Identify the parasite.
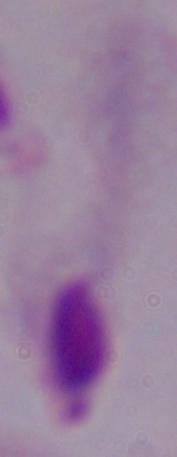
This is a trichomonad.

magnification = 1000x
modality = micrograph